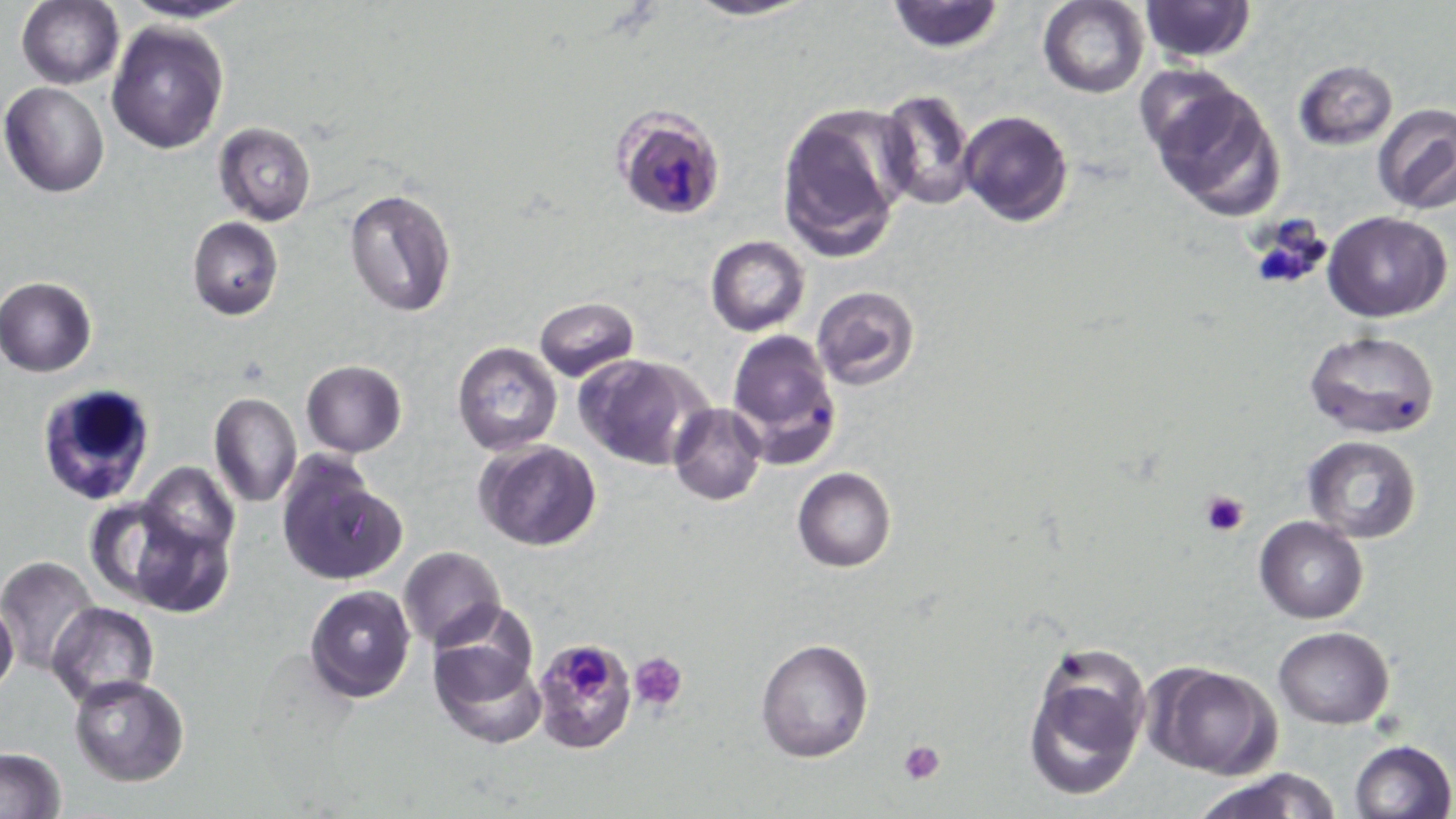 Approximate bounding boxes as named x1/y1/x2/y2 corners in pixels. Platelet locations: (x1=1244, y1=214, x2=1335, y2=293), (x1=1199, y1=488, x2=1250, y2=537), (x1=631, y1=651, x2=689, y2=710), (x1=898, y1=739, x2=947, y2=784). Uninfected red blood cell locations: (x1=116, y1=0, x2=259, y2=25), (x1=681, y1=0, x2=819, y2=22), (x1=886, y1=0, x2=1003, y2=52), (x1=1139, y1=0, x2=1257, y2=63), (x1=17, y1=1, x2=123, y2=89), (x1=1038, y1=1, x2=1149, y2=98), (x1=107, y1=20, x2=228, y2=154), (x1=1290, y1=59, x2=1398, y2=150), (x1=1130, y1=63, x2=1247, y2=165), (x1=1, y1=81, x2=111, y2=198), (x1=1146, y1=82, x2=1287, y2=224), (x1=875, y1=90, x2=977, y2=210), (x1=775, y1=104, x2=911, y2=262), (x1=1373, y1=105, x2=1456, y2=214), (x1=958, y1=109, x2=1073, y2=228), (x1=214, y1=122, x2=316, y2=225), (x1=344, y1=187, x2=458, y2=318), (x1=1324, y1=211, x2=1452, y2=322), (x1=187, y1=217, x2=283, y2=321), (x1=706, y1=236, x2=810, y2=336), (x1=0, y1=277, x2=98, y2=376), (x1=811, y1=286, x2=921, y2=391), (x1=533, y1=296, x2=639, y2=383), (x1=725, y1=328, x2=842, y2=466), (x1=1303, y1=328, x2=1440, y2=440), (x1=452, y1=342, x2=562, y2=455), (x1=576, y1=353, x2=711, y2=471), (x1=300, y1=359, x2=405, y2=457), (x1=209, y1=390, x2=300, y2=507), (x1=667, y1=402, x2=766, y2=506), (x1=1303, y1=437, x2=1423, y2=545), (x1=477, y1=441, x2=603, y2=550), (x1=276, y1=456, x2=404, y2=585), (x1=137, y1=463, x2=240, y2=565), (x1=793, y1=467, x2=896, y2=572), (x1=1255, y1=516, x2=1368, y2=622), (x1=133, y1=518, x2=232, y2=618), (x1=399, y1=546, x2=506, y2=649), (x1=0, y1=555, x2=100, y2=674), (x1=306, y1=584, x2=415, y2=701), (x1=0, y1=599, x2=19, y2=697), (x1=48, y1=602, x2=159, y2=706), (x1=1272, y1=625, x2=1393, y2=729), (x1=429, y1=626, x2=547, y2=748), (x1=755, y1=638, x2=874, y2=762), (x1=1021, y1=641, x2=1152, y2=803), (x1=1147, y1=662, x2=1281, y2=779), (x1=69, y1=675, x2=192, y2=785), (x1=1348, y1=739, x2=1455, y2=819), (x1=0, y1=748, x2=67, y2=819), (x1=1191, y1=768, x2=1343, y2=819). Plasmodium falciparum-infected red blood cell locations: (x1=612, y1=106, x2=728, y2=224), (x1=531, y1=635, x2=639, y2=753). White blood cell locations: (x1=36, y1=383, x2=160, y2=508). Slide-level diagnosis: Plasmodium falciparum. 1000x magnification. Light microscopy. Single field of view. Image is 1456×819 pixels. May-Grünwald-Giemsa-stained preparation. Thin blood film.